Classify this cell by malaria status.
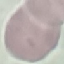

It is uninfected.

stain: Giemsa
capture: smartphone camera at the microscope eyepiece
image_type: cell patch, automatically extracted from a larger field of view and resized to 64 × 64 pixels
preparation: thin blood smear